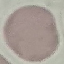 Malaria status: uninfected. Automatically extracted cell patch, resized to 64 × 64 pixels. Acquired by smartphone through the microscope eyepiece. Giemsa stain. Thin smear of blood.